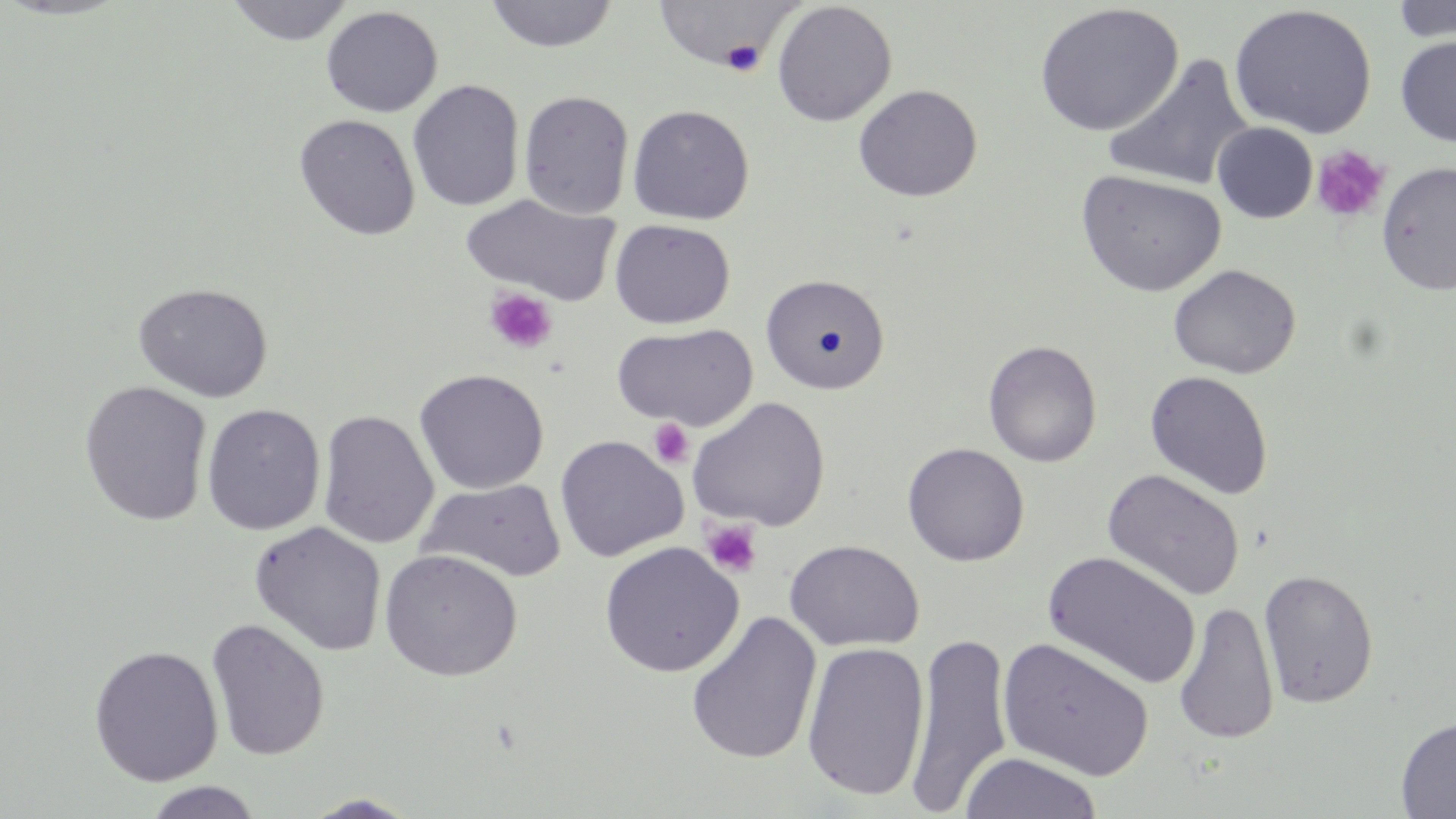
Approximate bounding boxes as (x1,y1)-(x2,y2) corner pairs in pixels. Uninfected red blood cell locations: (225,0)-(354,45), (1389,0)-(1456,44), (485,1)-(619,53), (653,1)-(800,70), (772,2)-(897,127), (1033,3)-(1185,137), (1229,4)-(1377,139), (321,5)-(443,118), (1395,35)-(1456,147), (1102,53)-(1255,192), (407,79)-(525,212), (853,84)-(982,202), (518,89)-(635,219), (627,104)-(755,225), (293,113)-(421,241), (1212,122)-(1318,223), (1376,161)-(1456,295), (1075,169)-(1226,297), (462,193)-(620,305), (610,219)-(735,329), (1167,263)-(1302,379), (760,273)-(890,394), (132,282)-(274,402), (612,322)-(759,430), (983,340)-(1102,467), (414,368)-(549,494), (1144,370)-(1274,499), (78,380)-(213,526), (688,397)-(830,531), (201,404)-(326,535), (317,410)-(438,549), (555,435)-(688,562), (902,442)-(1029,566), (1102,469)-(1246,602), (418,479)-(566,582), (249,521)-(387,656), (785,540)-(924,652), (599,541)-(744,678), (379,549)-(523,682), (1042,550)-(1202,691), (1258,569)-(1379,709), (1174,601)-(1279,744), (685,610)-(822,765), (206,618)-(330,761), (906,631)-(1014,815), (998,637)-(1154,781), (801,641)-(930,803), (89,644)-(223,786), (1396,716)-(1456,818), (959,751)-(1104,819), (143,781)-(263,819), (302,793)-(422,818). Platelet locations: (720,41)-(765,77), (1311,144)-(1390,222), (483,287)-(557,354), (649,418)-(694,469), (701,520)-(763,577). Slide-level diagnosis: negative for blood parasites. Single field of view. Optical microscopy. 1000x magnification. Image is 1456×819 pixels. May-Grünwald-Giemsa stain. Thin blood smear.